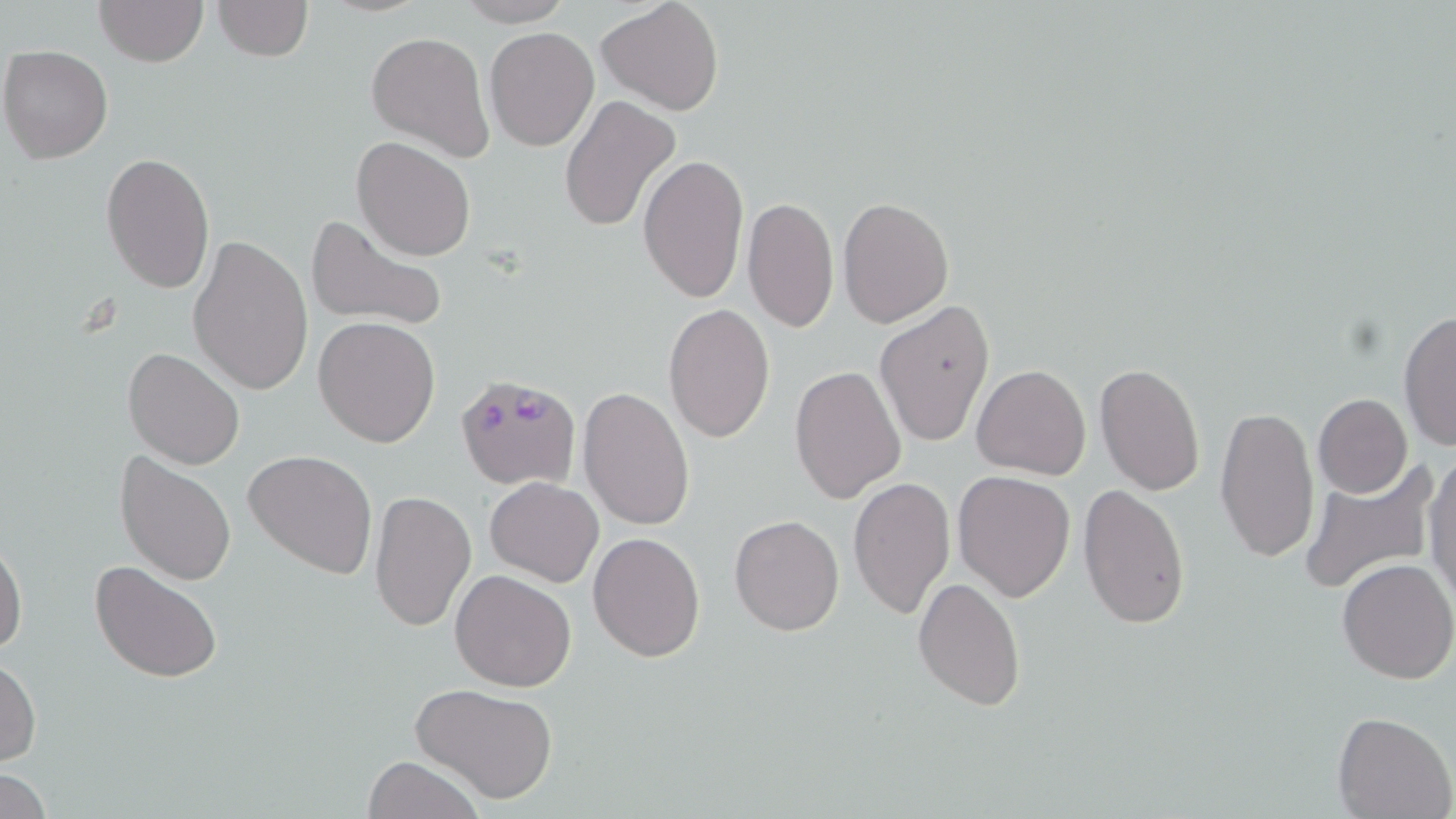

Summary:
  - Coordinate format: approximate bounding boxes as named x1/y1/x2/y2 corners in pixels
  - Plasmodium falciparum-infected red blood cell locations: (x1=453, y1=375, x2=583, y2=491)
  - Uninfected red blood cell locations: (x1=95, y1=0, x2=208, y2=67), (x1=210, y1=0, x2=314, y2=63), (x1=596, y1=0, x2=724, y2=116), (x1=455, y1=1, x2=575, y2=26), (x1=485, y1=26, x2=599, y2=151), (x1=365, y1=31, x2=494, y2=160), (x1=1, y1=45, x2=114, y2=163), (x1=559, y1=95, x2=680, y2=235), (x1=350, y1=135, x2=477, y2=261), (x1=100, y1=152, x2=214, y2=294), (x1=638, y1=154, x2=749, y2=304), (x1=742, y1=196, x2=838, y2=336), (x1=837, y1=197, x2=953, y2=327), (x1=304, y1=213, x2=448, y2=336), (x1=187, y1=232, x2=312, y2=397), (x1=875, y1=302, x2=998, y2=448), (x1=664, y1=303, x2=775, y2=442), (x1=1397, y1=309, x2=1455, y2=450), (x1=316, y1=316, x2=439, y2=448), (x1=122, y1=347, x2=245, y2=469), (x1=1094, y1=363, x2=1207, y2=497), (x1=971, y1=364, x2=1090, y2=480), (x1=789, y1=365, x2=906, y2=503), (x1=577, y1=385, x2=697, y2=530), (x1=1313, y1=394, x2=1412, y2=498), (x1=1214, y1=403, x2=1318, y2=565), (x1=114, y1=450, x2=237, y2=587), (x1=243, y1=451, x2=378, y2=579), (x1=1425, y1=451, x2=1456, y2=606), (x1=1297, y1=460, x2=1437, y2=596), (x1=952, y1=470, x2=1076, y2=601), (x1=848, y1=476, x2=954, y2=618), (x1=485, y1=477, x2=604, y2=587), (x1=1079, y1=484, x2=1190, y2=630), (x1=370, y1=490, x2=477, y2=633), (x1=729, y1=514, x2=844, y2=637), (x1=588, y1=532, x2=705, y2=661), (x1=0, y1=537, x2=27, y2=658), (x1=89, y1=558, x2=222, y2=683), (x1=1335, y1=558, x2=1456, y2=685), (x1=449, y1=568, x2=577, y2=693), (x1=912, y1=577, x2=1027, y2=711), (x1=0, y1=656, x2=41, y2=767), (x1=409, y1=682, x2=559, y2=804), (x1=1331, y1=710, x2=1455, y2=819), (x1=362, y1=756, x2=485, y2=819)
  - Slide-level diagnosis: Plasmodium falciparum
  - Preparation: thin blood smear
  - Image size: 1456×819 pixels
  - Magnification: 1000x
  - Modality: light microscopy
  - Stain: May-Grünwald-Giemsa
  - Field of view: single